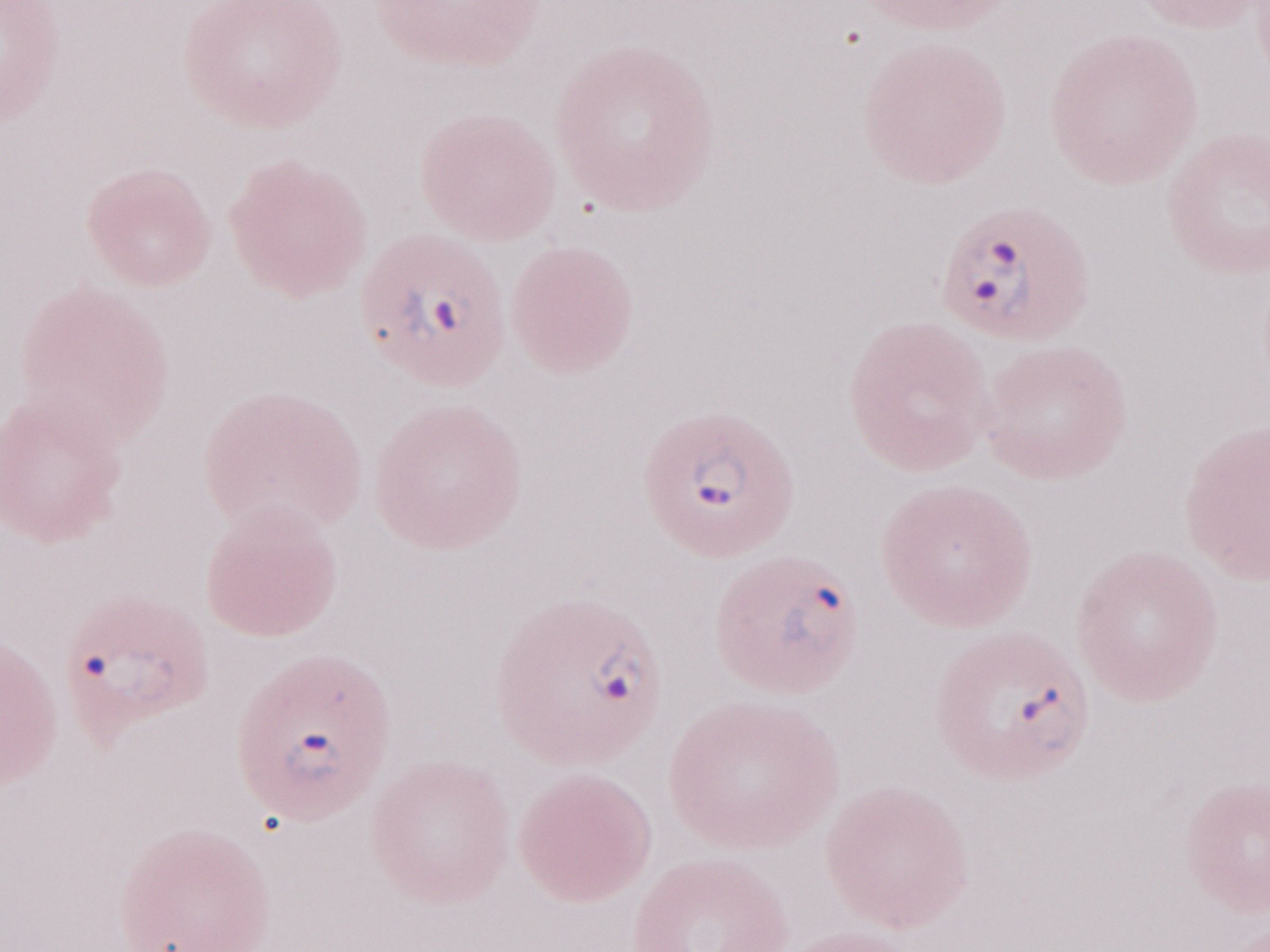 One field of this slide. Image is 1270×952 pixels. Malaria diagnosis (patient-level): positive. May-Grünwald-Giemsa (MGG) stain. Olympus BX43 microscope, Olympus DP73 camera. Magnification: 1,000x. Thin peripheral-blood smear.